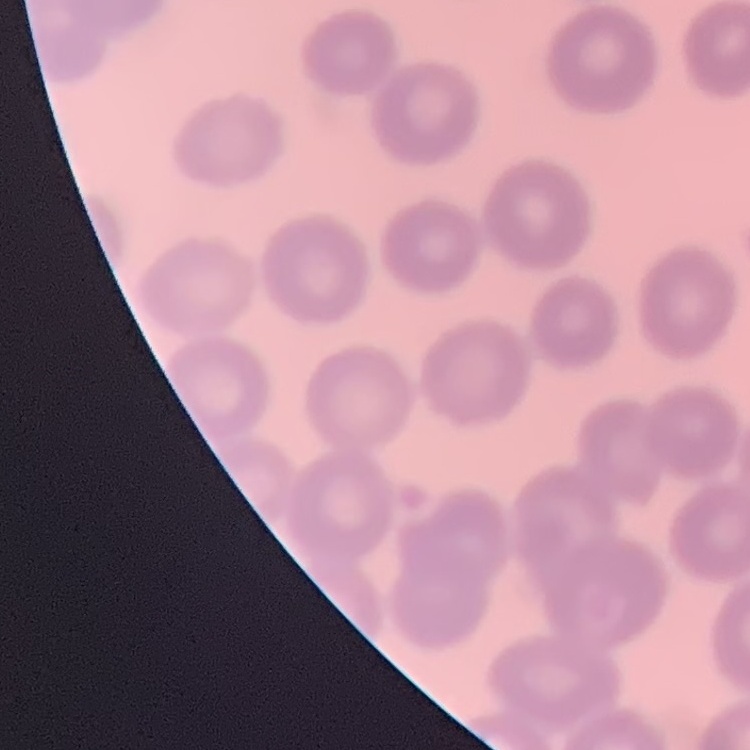
red blood cell morphology = no rouleaux formation
image type = square crop of a larger photomicrograph
preparation = thin peripheral smear
stain = Field's or Giemsa